Point out each malaria parasite.
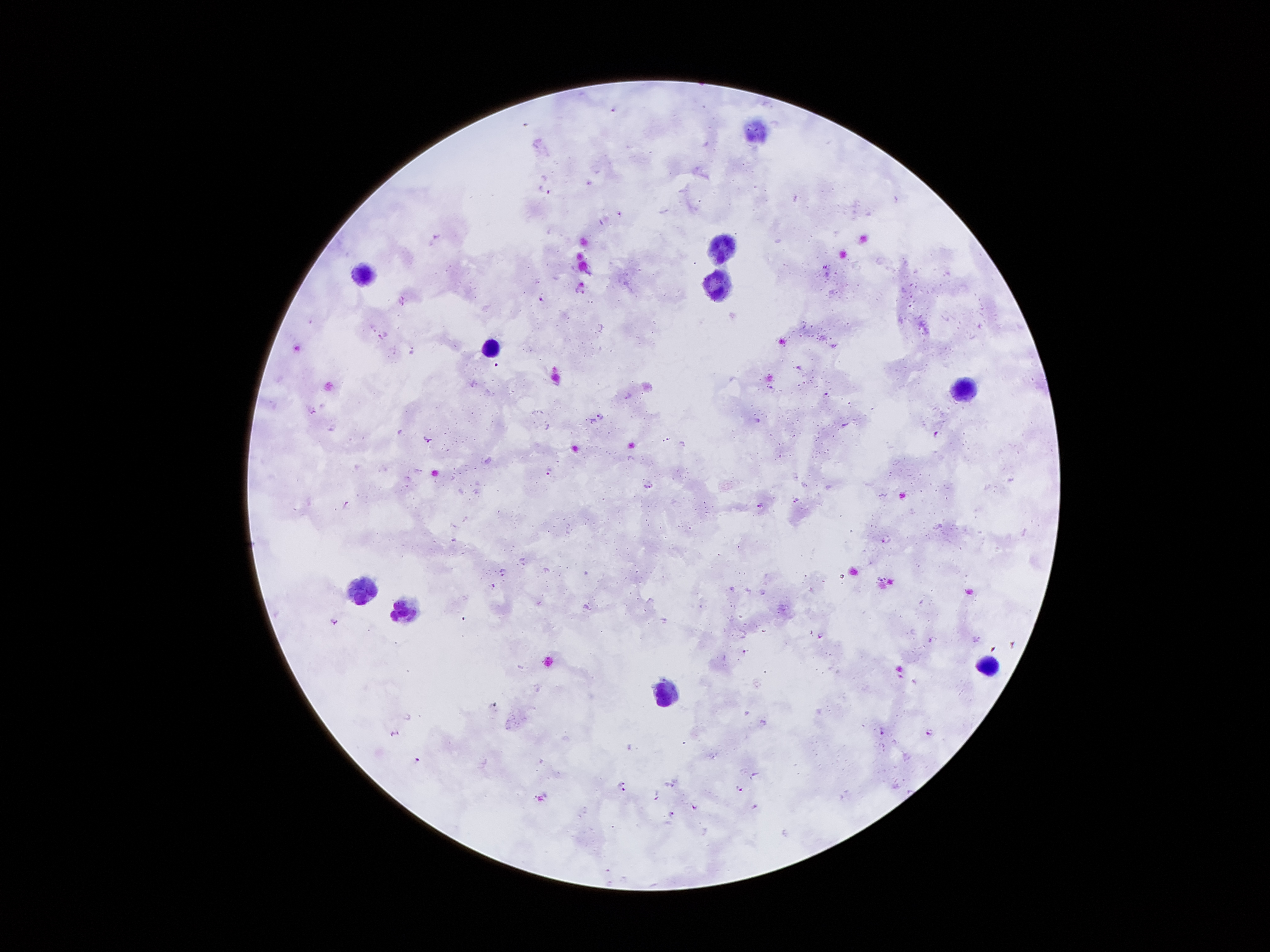
Approximate centers as {x, y} in pixels.
Malaria parasites: {612, 109}, {544, 188}, {795, 198}, {896, 199}, {618, 212}, {435, 236}, {825, 267}, {581, 292}, {541, 298}, {401, 300}, {309, 321}, {380, 335}, {412, 349}, {799, 365}, {473, 383}, {825, 394}, {627, 395}, {312, 410}, {600, 414}, {592, 420}, {757, 420}, {844, 424}, {545, 425}, {330, 427}, {934, 433}, {666, 438}, {427, 439}, {682, 443}, {417, 470}, {547, 471}, {803, 484}, {647, 485}, {796, 499}, {344, 502}, {759, 505}, {453, 538}, {884, 538}, {502, 568}, {547, 570}, {492, 583}, {730, 588}, {763, 592}, {587, 606}, {334, 619}, {665, 620}, {820, 633}, {931, 637}, {744, 650}, {900, 674}, {763, 722}, {882, 729}, {928, 730}, {394, 733}, {416, 758}, {753, 774}, {622, 782}, {670, 784}, {739, 788}, {624, 789}, {656, 796}, {693, 806}, {754, 806}, {671, 812}.

Leukocyte locations: {755, 132}, {722, 246}, {363, 276}, {719, 285}, {490, 349}, {963, 387}, {356, 587}, {405, 610}, {986, 666}, {664, 695}. Single field of view. Patient malaria status: positive for Plasmodium falciparum. Smartphone photograph taken through the microscope eyepiece. Giemsa stain. 100x magnification. Thick peripheral-blood smear. Image is 1270×952 pixels.